Assess this cell for malaria.
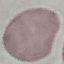

It is uninfected.

Summary:
  - Capture: smartphone through the microscope eyepiece
  - Stain: Giemsa
  - Image type: cell patch, automatically extracted from a larger field of view and resized to 64 × 64 pixels
  - Preparation: thin blood smear